Comment on the morphology of the erythrocytes.
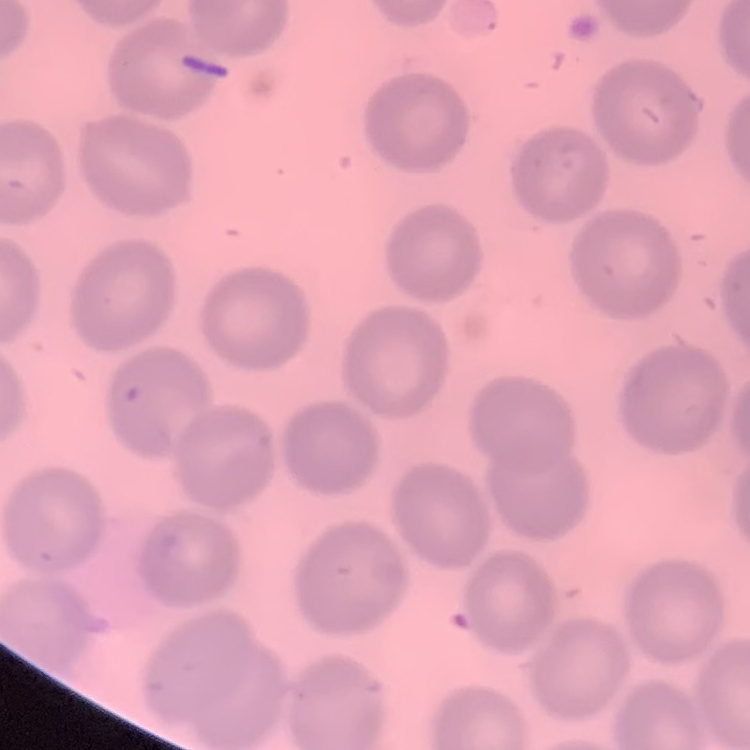

They show no rouleaux formation.

{
  "image_type": "one tile cut from a larger photomicrograph",
  "stain": "Field's or Giemsa",
  "preparation": "thin blood smear"
}